Assess this cell for malaria.
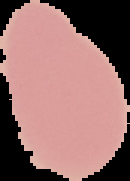

It is uninfected.

Summary:
  - Preparation: thin blood film
  - Image type: cell region segmented out of the field of view; surrounding area masked to black
  - Image size: 130×181 pixels